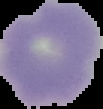

Summary:
  - Result: no Plasmodium parasites seen
  - Image type: cell region segmented out of the field of view; surrounding area masked to black
  - Preparation: thin blood smear
  - Image size: 103×109 pixels